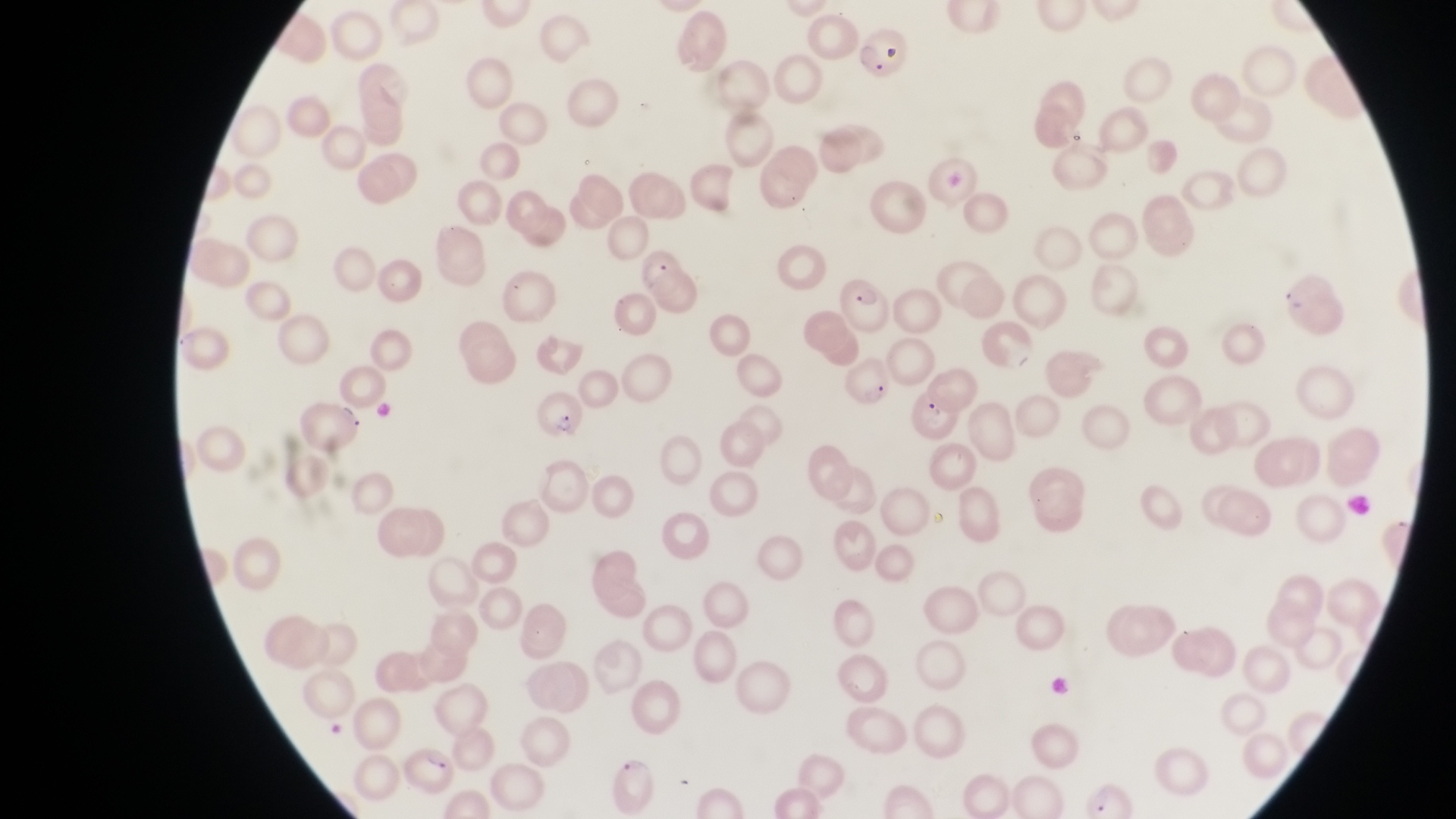

Approximate bounding boxes as {left, top, right, bottom} in pixels.
Summary:
  - Parasitised red blood cell locations: {848, 24, 906, 79}, {840, 275, 899, 336}, {843, 357, 895, 406}, {296, 394, 369, 454}, {534, 396, 581, 439}, {404, 748, 454, 797}
  - Country: Uganda
  - Capture: smartphone photograph through the eyepiece of an Olympus CX-23 microscope
  - Preparation: thin blood smear
  - Image size: 1456×819 pixels
  - Field of view: single
  - Magnification: 1000x